Point out each malaria parasite.
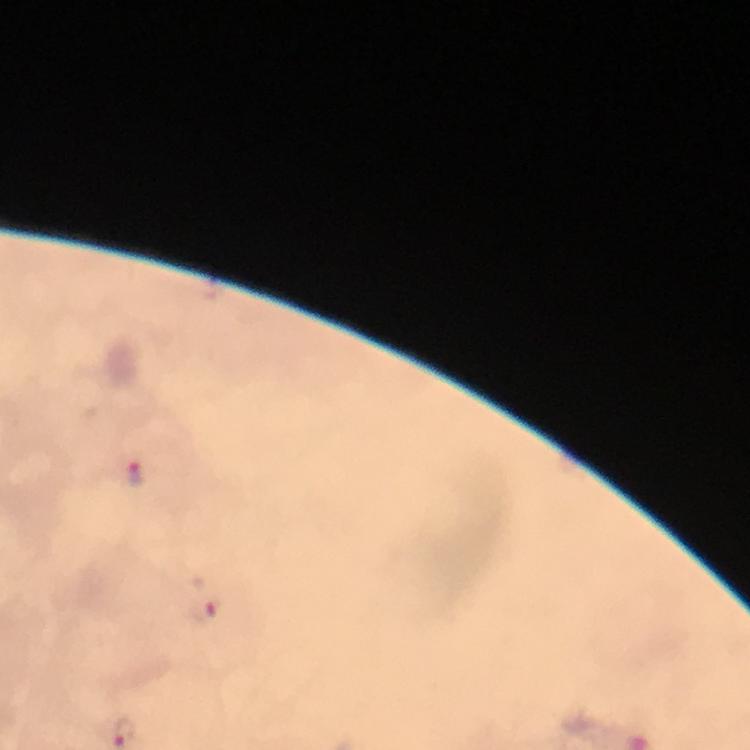

Approximate centers as [x, y] in pixels.
Malaria parasites: [134, 472], [205, 609].

stain = Giemsa
cropped from = one field of view
immersion oil = applied
capture = smartphone camera through the microscope
magnification = 100x
preparation = thick blood film
context = from a diagnostic examination for malaria
image size = 750×750 pixels